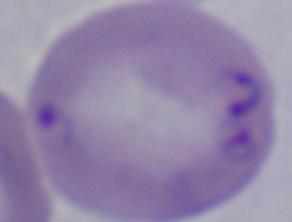
{
  "identification": "Babesia",
  "modality": "micrograph",
  "magnification": "1000x"
}